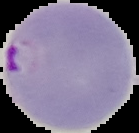
malaria status = parasitized
image size = 139×133 pixels
image type = cell region segmented out of the field of view; surrounding area masked to black
preparation = thin blood smear